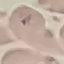

Summary:
  - Malaria status: uninfected
  - Stain: Giemsa
  - Capture: smartphone through the microscope eyepiece
  - Image type: automatically extracted cell patch, resized to 64 × 64 pixels
  - Preparation: thin smear